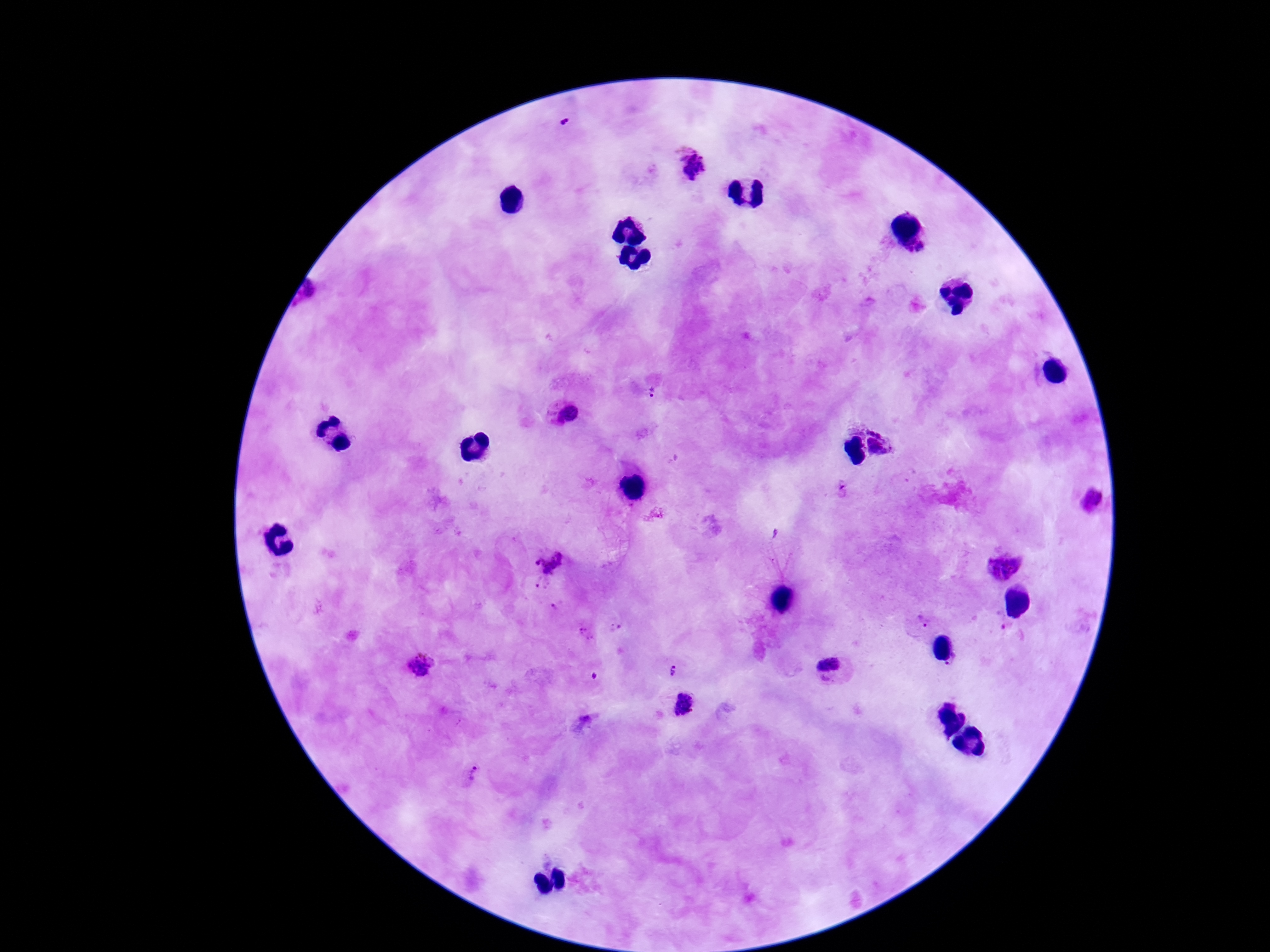
preparation: thick blood film
field_of_view: single
capture: smartphone camera through the microscope eyepiece
stain: Giemsa
plasmodium_parasite_locations: 'approximate centers as [x, y] in pixels: [567, 124], [690, 163], [924, 248], [651, 392], [565, 414], [884, 440], [845, 490], [1089, 500], [1004, 563], [548, 564], [541, 586], [557, 609], [924, 622], [1007, 627], [617, 629], [588, 636], [954, 663], [419, 667], [833, 670], [672, 672], [683, 703], [581, 725], [472, 773]'
magnification: 100x
image_size: 1270×952 pixels
patient_malaria_status: positive